Assess for malaria.
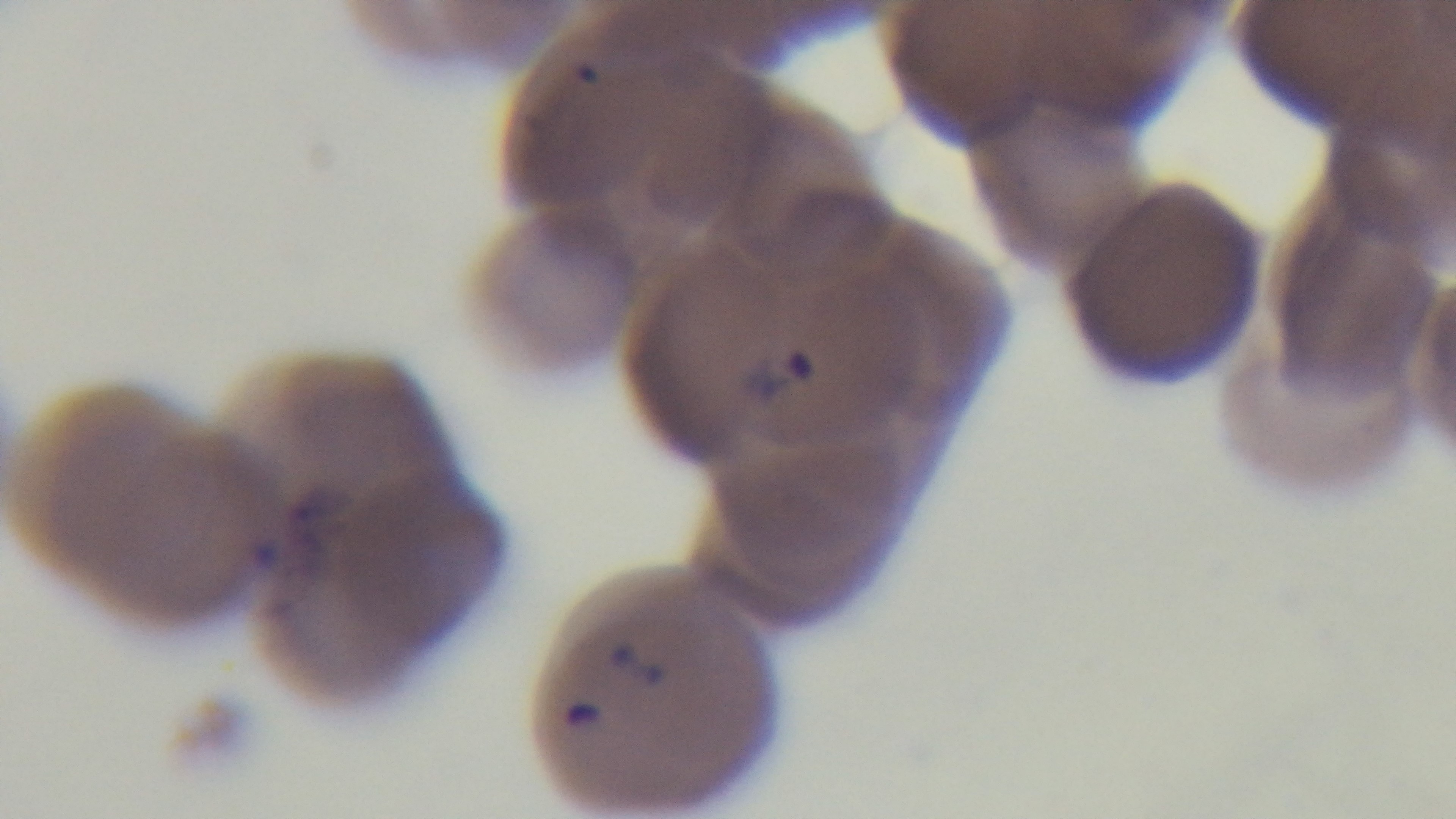

Positive.

capture = mounted 4K digital camera
objective = 100x oil immersion
stain = Giemsa
preparation = thin
field of view = one from the slide
modality = light microscopy